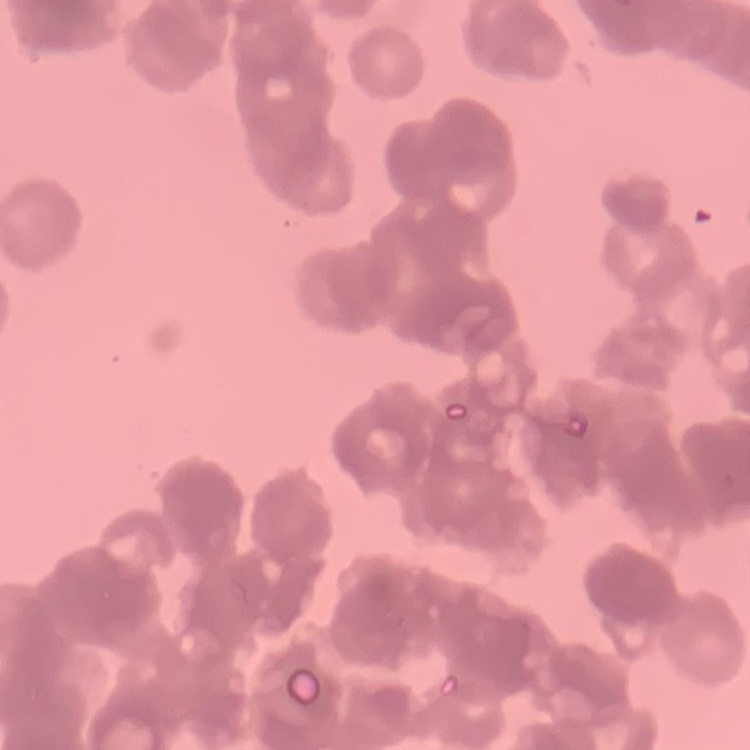
The red blood cells show rouleaux formation. Field's or Giemsa stain. Square crop of a larger photomicrograph. Thin blood film.